Locate every P. falciparum parasite and give its life-cycle stage, and locate every leukocyte and any debris.
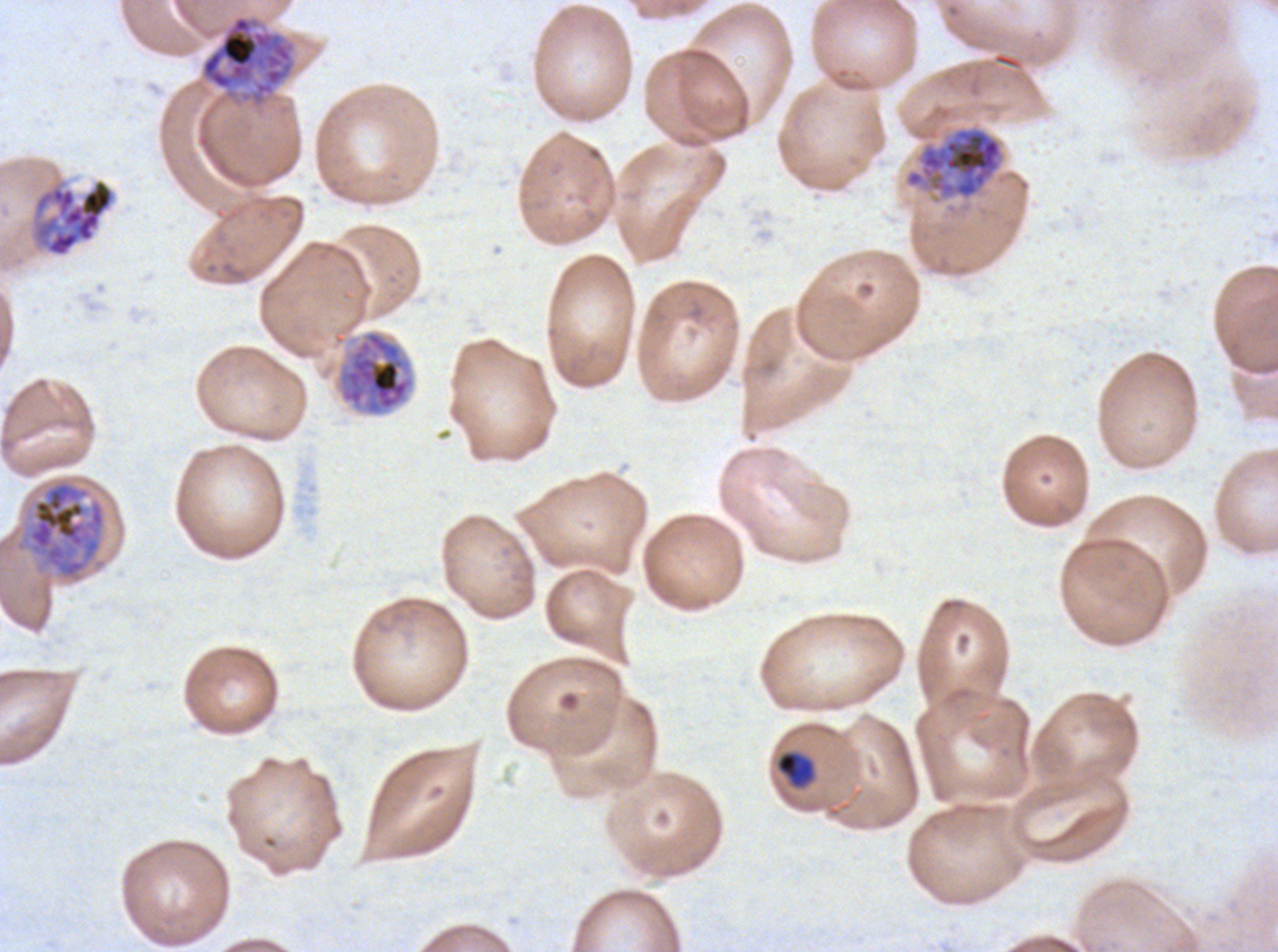
Approximate bounding boxes as (x1, y1, x2, y2) in pixels.
Late-ring/early-trophozoite forms: (775, 751, 816, 788).
Early schizonts: (200, 14, 296, 108), (903, 125, 1005, 201), (31, 177, 117, 258), (336, 329, 415, 417), (27, 480, 106, 580).
No rings, mid trophozoites, late trophozoites, late schizonts, segmenters, gametocytes, leukocytes, or debris observed.

stain = Giemsa
specimen = ex-vivo P. falciparum culture from a patient in The Gambia, grown for 24 to 48 hours
field of view = sub-image separated from a larger composite
life-cycle stages observed = late-ring/early-trophozoite, early schizont
preparation = thin blood film
image size = 1278×952 pixels